Comment on the morphology of the erythrocytes.
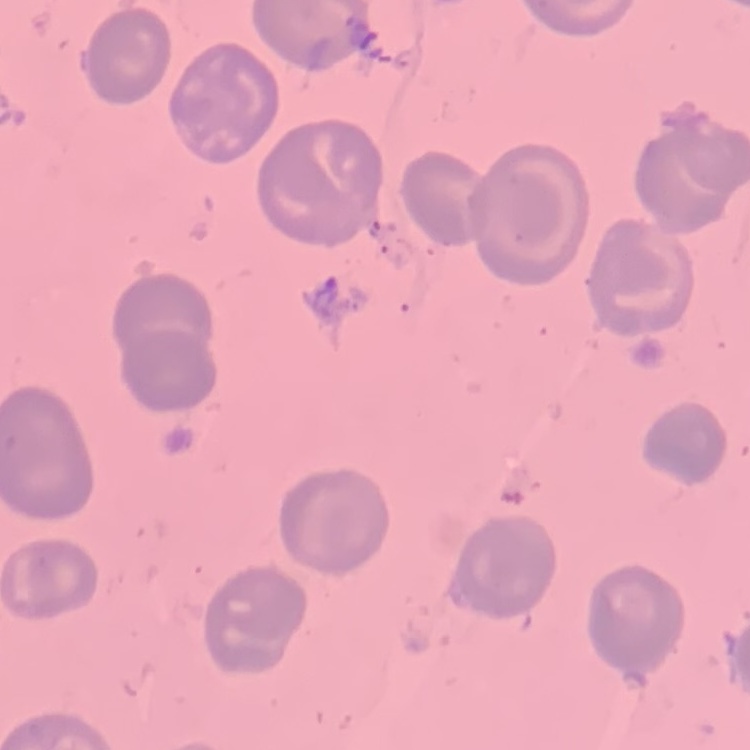
No rouleaux formation.

image_type: square crop of a larger photomicrograph
preparation: thin blood film
stain: Field's or Giemsa